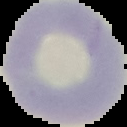

image type = cell region segmented out of the field of view; surrounding area masked to black
image size = 127×127 pixels
preparation = thin blood film
malaria status = uninfected